Classify this cell by malaria status.
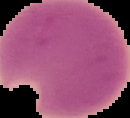

It is parasitized.

Summary:
  - Image type: segmented cell region with the area outside set to black
  - Preparation: thin blood film
  - Image size: 130×118 pixels